Assess this cell for malaria.
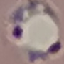

Parasitized.

Summary:
  - Preparation: thin smear
  - Stain: Giemsa
  - Capture: smartphone through the microscope eyepiece
  - Image type: automatically extracted cell patch, resized to 64 × 64 pixels